Look for Plasmodium parasites.
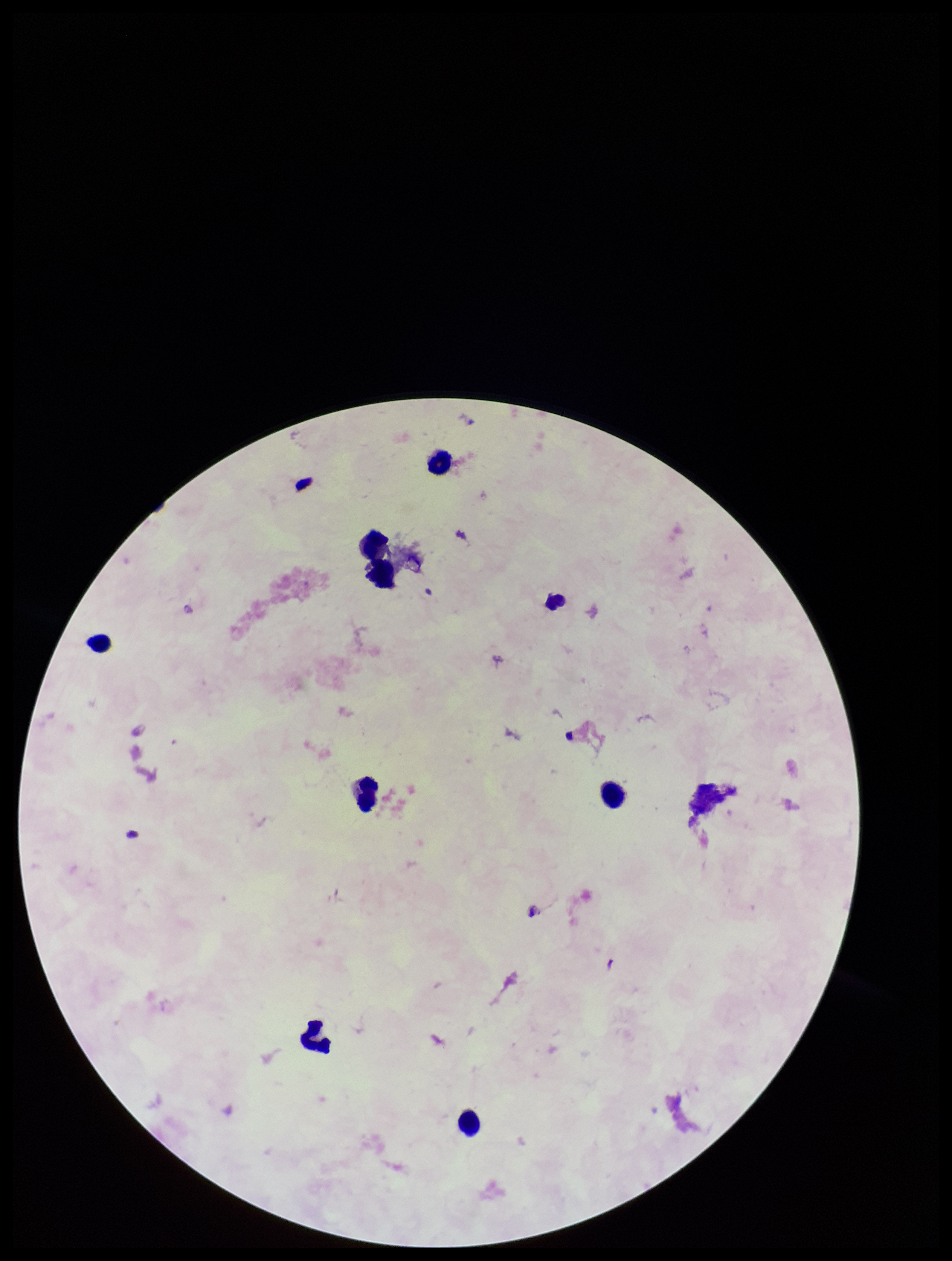

None seen.

Summary:
  - Preparation: thick
  - Parasite count: 0
  - Patient malaria status: negative
  - Capture: smartphone photograph through the microscope eyepiece
  - Field of view: one from this slide
  - Stain: Giemsa
  - Leukocyte count: 8
  - Image size: 952×1261 pixels